Classify this cell by malaria status.
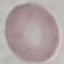

Uninfected.

Summary:
  - Stain: Giemsa
  - Image type: automatically extracted cell patch, resized to 64 × 64 pixels
  - Capture: smartphone camera at the microscope eyepiece
  - Preparation: thin smear